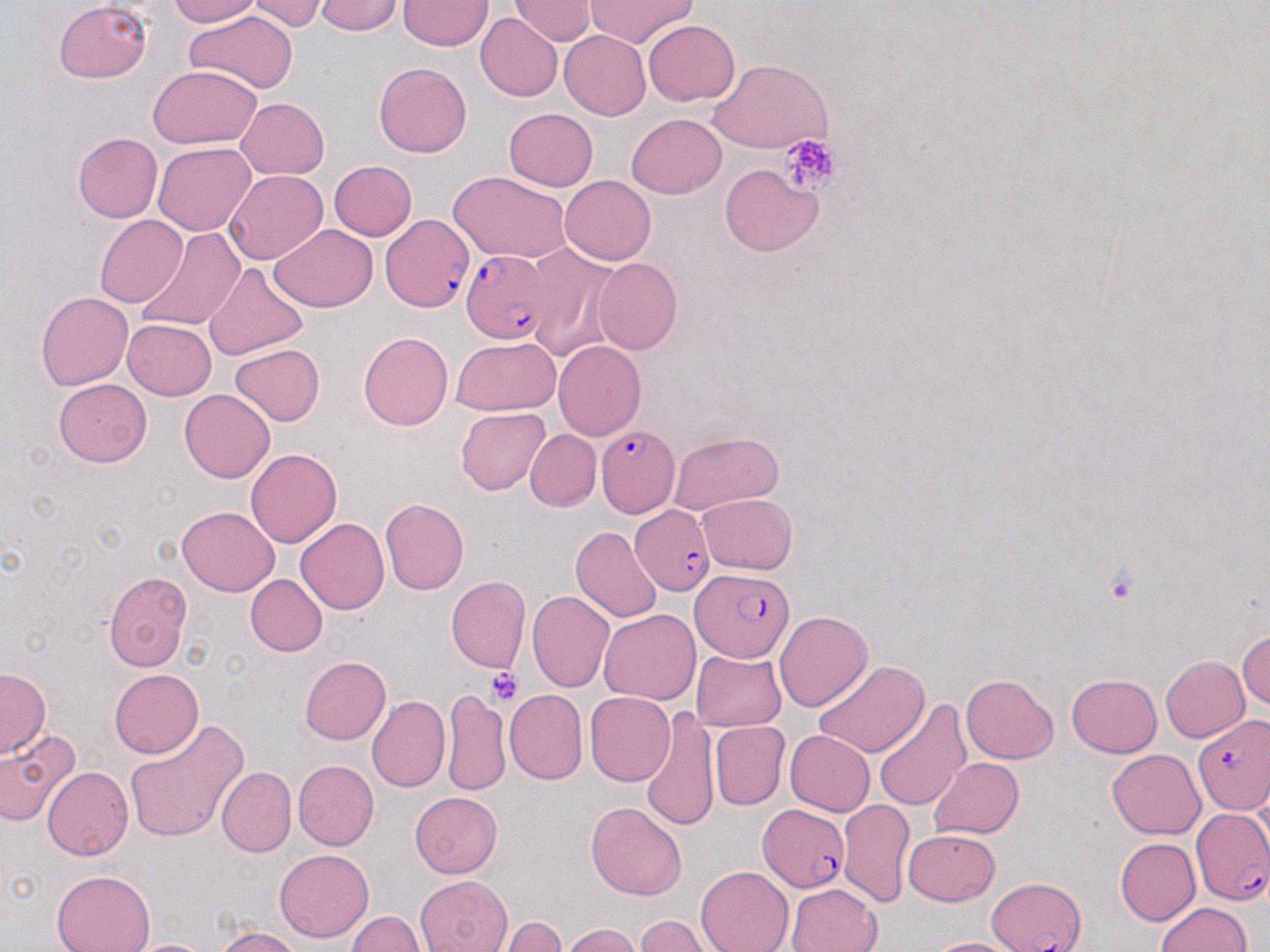

Approximate bounding boxes as (x1, y1, x2, y2) in pixels. Plasmodium falciparum-infected red blood cell locations: (382, 211, 472, 314), (462, 249, 552, 344), (596, 424, 678, 520), (630, 505, 715, 595), (690, 569, 791, 660), (1192, 716, 1270, 815), (757, 804, 848, 892), (1191, 808, 1270, 906), (990, 876, 1086, 951). Uninfected red blood cell locations: (167, 0, 262, 25), (249, 0, 328, 32), (510, 0, 597, 45), (586, 0, 697, 48), (54, 1, 152, 83), (314, 1, 404, 35), (399, 1, 492, 50), (185, 10, 297, 93), (475, 13, 563, 101), (643, 19, 740, 105), (560, 31, 651, 120), (710, 59, 831, 154), (374, 61, 472, 158), (149, 65, 261, 148), (235, 98, 329, 179), (504, 108, 598, 191), (627, 113, 726, 198), (73, 132, 161, 222), (153, 144, 255, 235), (327, 160, 417, 240), (719, 163, 823, 257), (225, 170, 326, 263), (449, 171, 573, 264), (560, 175, 655, 264), (94, 214, 187, 307), (269, 224, 377, 311), (134, 226, 245, 334), (525, 244, 620, 361), (593, 257, 682, 355), (203, 262, 309, 362), (35, 292, 132, 390), (122, 318, 217, 400), (359, 332, 454, 431), (449, 337, 560, 416), (553, 341, 646, 441), (230, 343, 326, 426), (53, 379, 151, 466), (179, 389, 274, 483), (455, 407, 551, 496), (526, 429, 601, 511), (667, 432, 783, 515), (245, 448, 342, 548), (697, 494, 798, 575), (379, 498, 469, 595), (177, 506, 279, 596), (295, 518, 389, 614), (570, 527, 663, 623), (103, 571, 192, 672), (245, 575, 327, 656), (446, 576, 529, 673), (527, 590, 614, 691), (599, 609, 700, 705), (773, 612, 872, 712), (1236, 630, 1269, 711), (691, 650, 786, 731), (1161, 654, 1249, 742), (299, 656, 391, 745), (814, 660, 928, 757), (1, 667, 51, 759), (109, 668, 202, 757), (1067, 673, 1161, 757), (961, 674, 1058, 764), (439, 687, 510, 798), (504, 689, 588, 784), (585, 691, 676, 786), (367, 695, 449, 793), (873, 699, 970, 810), (639, 704, 719, 832), (122, 721, 249, 843), (710, 721, 789, 810), (0, 730, 81, 826), (785, 730, 874, 816), (1108, 749, 1205, 838), (930, 758, 1024, 839), (292, 760, 379, 851), (43, 767, 133, 860), (216, 767, 296, 857), (409, 792, 502, 878), (837, 798, 914, 907), (587, 803, 687, 901), (904, 828, 999, 906), (1114, 838, 1201, 926), (274, 847, 374, 943), (694, 866, 792, 952), (51, 869, 155, 952), (417, 876, 512, 952), (786, 883, 882, 952), (1155, 901, 1251, 951), (347, 911, 425, 951), (636, 916, 712, 952), (501, 917, 569, 951), (560, 924, 643, 952), (213, 926, 300, 952), (924, 937, 1024, 952), (125, 938, 218, 951). Platelet locations: (779, 134, 841, 195), (1105, 565, 1138, 602), (486, 667, 524, 705). Slide-level diagnosis: Plasmodium falciparum. Light microscopy. Thin blood film. Captured at 1000x magnification. May-Grünwald-Giemsa-stained preparation. Single field of view. Image is 1270×952 pixels.